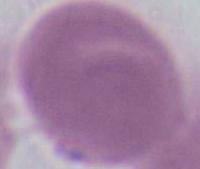
Summary:
  - Magnification: 1000x
  - Identification: erythrocyte
  - Modality: photomicrograph